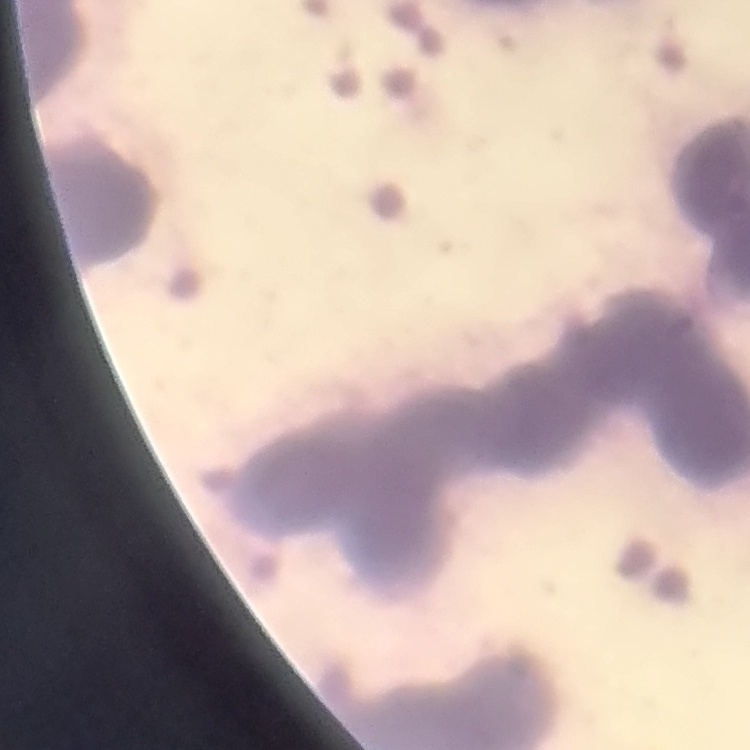
red blood cell morphology = rouleaux formation
preparation = thin blood film
stain = Field's or Giemsa
image type = square crop of a larger photomicrograph